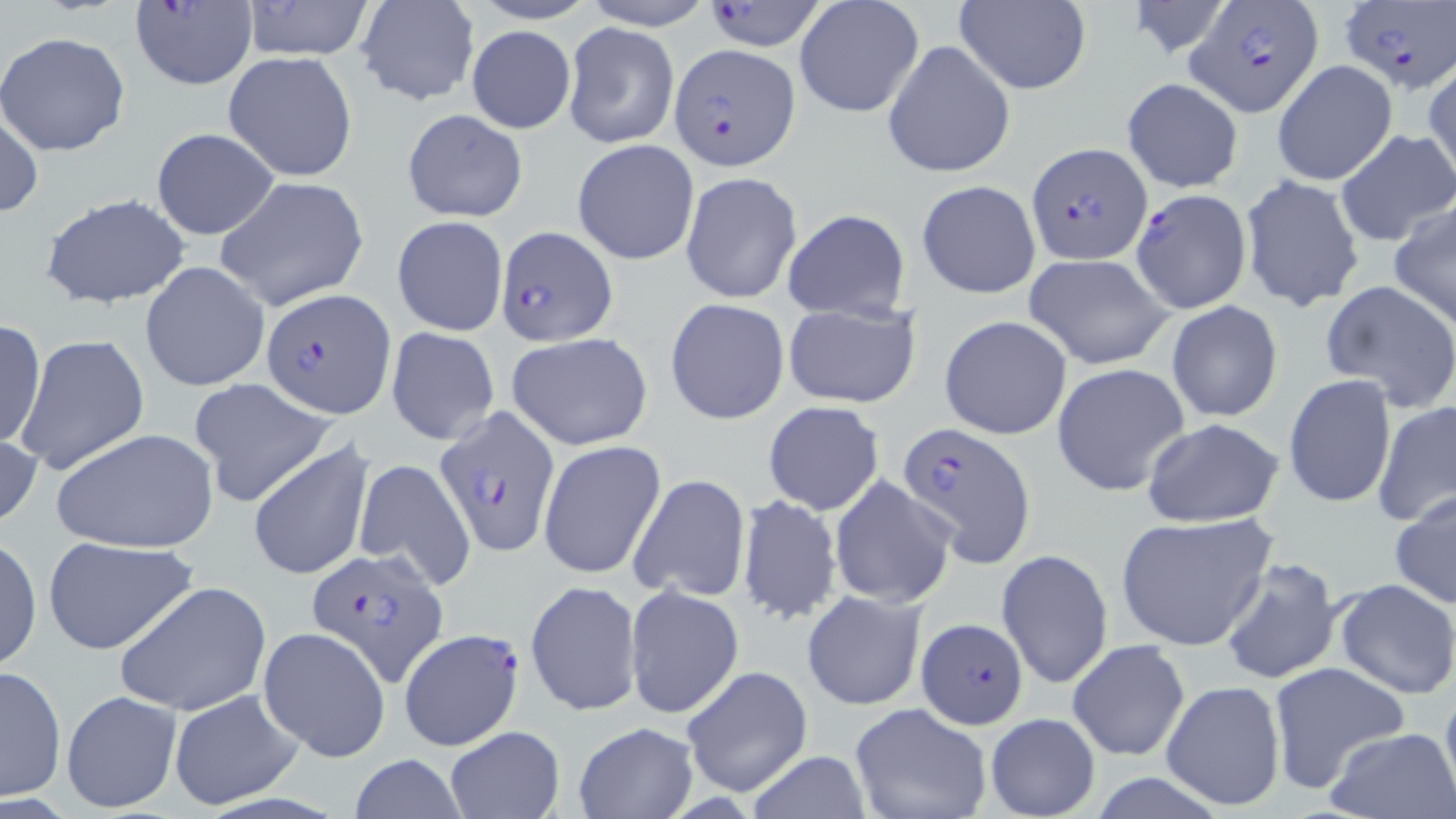

Approximate bounding boxes as [x1, y1, x2, y2] in pixels. Plasmodium falciparum-infected red blood cell locations: [697, 0, 834, 51], [1185, 0, 1325, 116], [1339, 0, 1455, 95], [128, 1, 259, 92], [668, 43, 799, 170], [1027, 143, 1150, 261], [1130, 187, 1251, 315], [496, 225, 616, 345], [262, 287, 394, 419], [433, 406, 564, 557], [895, 421, 1034, 568], [307, 546, 449, 687], [915, 618, 1028, 727], [398, 628, 525, 749]. Uninfected red blood cell locations: [240, 0, 377, 60], [579, 0, 717, 30], [795, 0, 925, 120], [952, 0, 1093, 96], [354, 1, 480, 106], [1124, 1, 1232, 59], [564, 22, 678, 150], [466, 26, 576, 133], [0, 31, 132, 158], [882, 39, 1016, 179], [222, 52, 358, 181], [1272, 60, 1398, 185], [1424, 62, 1456, 187], [1122, 77, 1243, 194], [1, 100, 43, 222], [401, 108, 529, 223], [151, 128, 280, 240], [1336, 128, 1456, 247], [573, 138, 700, 266], [680, 171, 803, 305], [1239, 172, 1365, 313], [214, 175, 370, 311], [917, 179, 1041, 300], [40, 193, 191, 309], [1389, 202, 1456, 330], [781, 208, 911, 321], [391, 215, 508, 337], [1025, 253, 1175, 369], [140, 260, 272, 392], [1321, 279, 1456, 415], [666, 298, 790, 425], [783, 301, 919, 409], [1166, 301, 1283, 422], [940, 315, 1073, 439], [0, 317, 46, 450], [386, 325, 500, 445], [505, 332, 653, 452], [14, 334, 150, 476], [1051, 363, 1190, 497], [1283, 374, 1396, 508], [189, 377, 338, 506], [1373, 400, 1456, 527], [762, 401, 885, 516], [1140, 419, 1285, 528], [0, 422, 43, 534], [51, 427, 218, 554], [538, 441, 667, 582], [250, 442, 374, 581], [352, 457, 476, 589], [627, 473, 751, 605], [829, 475, 957, 609], [1391, 490, 1456, 609], [736, 494, 842, 625], [1115, 512, 1276, 653], [1, 535, 42, 673], [43, 537, 199, 655], [996, 549, 1113, 689], [1218, 557, 1345, 684], [1333, 578, 1456, 700], [526, 579, 642, 718], [114, 580, 270, 716], [624, 584, 743, 718], [801, 590, 926, 711], [258, 626, 391, 762], [1066, 640, 1190, 761], [1267, 662, 1412, 795], [1, 664, 67, 800], [681, 666, 812, 797], [1439, 676, 1456, 806], [1161, 681, 1285, 809], [168, 688, 303, 810], [61, 689, 182, 814], [849, 702, 991, 819], [984, 711, 1100, 819], [572, 722, 698, 818], [1326, 727, 1456, 818], [443, 728, 565, 818], [749, 751, 870, 819], [347, 754, 471, 819]. Slide-level diagnosis: Plasmodium falciparum. One field of a larger specimen. Optical microscopy. 1000x magnification. Image is 1456×819 pixels. Thin blood smear. May-Grünwald-Giemsa stain.